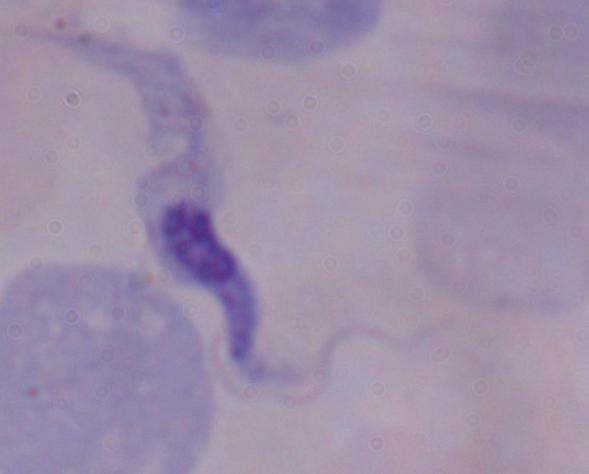
Summary:
  - Modality: micrograph
  - Identification: trypanosome
  - Magnification: 1000x